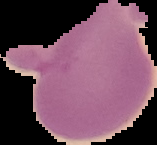
image size = 157×145 pixels
image type = cell region segmented out of the field of view; surrounding area masked to black
malaria status = uninfected
preparation = thin blood film